Comment on the morphology of the red blood cells.
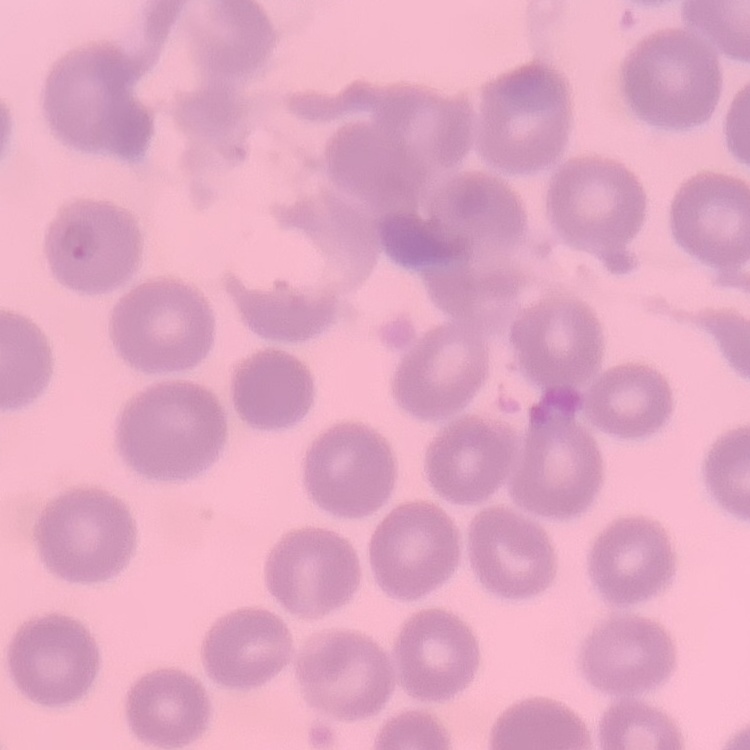

No rouleaux formation.

Stained with either Field's or Giemsa. Thin peripheral smear. One tile cut from a larger photomicrograph.